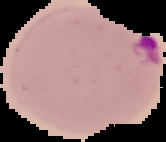
Summary:
  - Result: Plasmodium parasites identified
  - Preparation: thin blood film
  - Image size: 166×142 pixels
  - Image type: segmented cell region on a black background